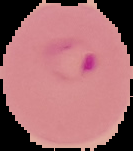

Image is 133×151 pixels. Cell region segmented out of the field of view; the surrounding area is masked to black. From a thin blood smear. Result: Plasmodium parasites detected.